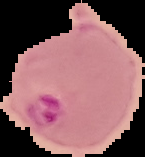 From a thin blood smear. Result: Plasmodium parasites detected. Image is 145×157 pixels. Cell region segmented out of the field of view; the surrounding area is masked to black.